Report the malaria status of this cell.
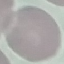
Uninfected.

Acquired by smartphone through the microscope eyepiece. Giemsa-stained preparation. Automatically extracted cell patch, resized to 64 × 64 pixels. Thin blood smear.